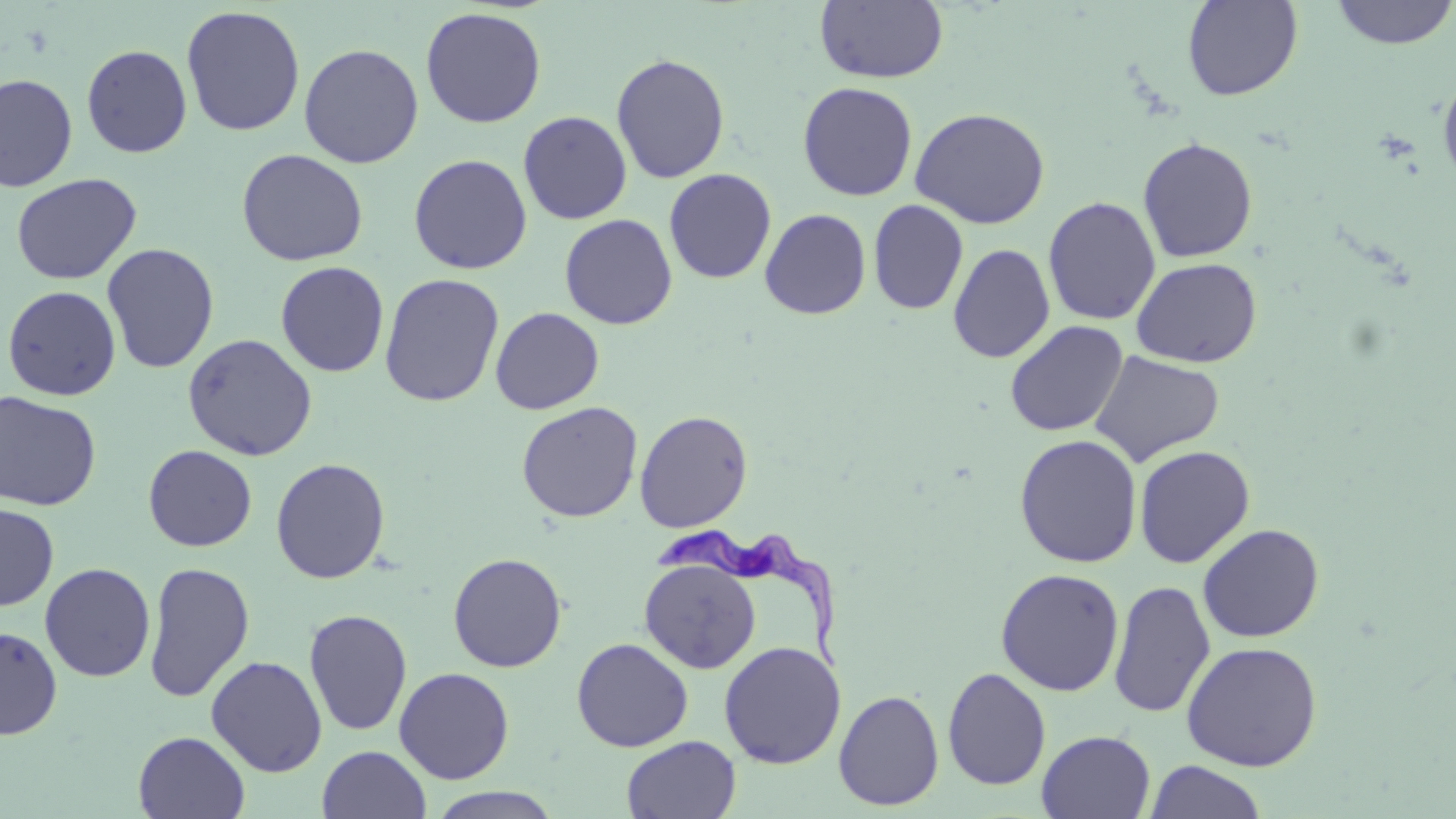

Summary:
  - Coordinate format: approximate bounding boxes as [x1, y1, x2, y2] in pixels
  - Trypanosoma brucei locations: [650, 527, 851, 676]
  - Uninfected red blood cell locations: [815, 0, 948, 84], [1181, 0, 1304, 101], [1330, 0, 1455, 50], [181, 5, 306, 137], [420, 6, 547, 129], [299, 43, 424, 168], [81, 44, 192, 158], [611, 53, 730, 184], [1437, 69, 1456, 190], [0, 73, 78, 192], [797, 81, 918, 201], [911, 107, 1050, 229], [518, 111, 632, 225], [1137, 137, 1258, 262], [236, 148, 368, 267], [409, 154, 532, 274], [663, 168, 777, 284], [11, 173, 142, 285], [1043, 196, 1161, 326], [868, 199, 968, 315], [759, 208, 871, 320], [559, 213, 678, 329], [101, 243, 219, 374], [948, 243, 1055, 363], [1131, 257, 1262, 368], [275, 261, 389, 377], [379, 273, 505, 407], [2, 285, 121, 401], [490, 307, 604, 414], [1005, 320, 1129, 438], [182, 333, 318, 461], [1089, 350, 1225, 467], [0, 390, 101, 511], [516, 402, 643, 522], [634, 409, 754, 532], [1014, 434, 1142, 568], [142, 444, 257, 552], [1134, 444, 1255, 568], [270, 458, 391, 584], [0, 503, 59, 611], [1198, 523, 1325, 642], [447, 552, 567, 672], [639, 557, 761, 674], [143, 561, 255, 703], [39, 562, 156, 682], [995, 568, 1125, 696], [1108, 579, 1215, 718], [304, 608, 413, 736], [0, 625, 62, 739], [571, 637, 693, 752], [1181, 640, 1323, 772], [719, 641, 845, 769], [206, 655, 327, 777], [393, 666, 514, 784], [942, 667, 1051, 791], [833, 689, 944, 811], [1037, 730, 1156, 819], [133, 731, 250, 818], [621, 735, 741, 819], [317, 745, 431, 819], [1144, 760, 1268, 819], [426, 787, 564, 818]
  - Slide-level diagnosis: Trypanosoma brucei
  - Field of view: one of a larger specimen
  - Magnification: 1000x
  - Preparation: thin blood film
  - Image size: 1456×819 pixels
  - Stain: May-Grünwald-Giemsa
  - Modality: optical microscopy